Locate every blood parasite and identify its species.
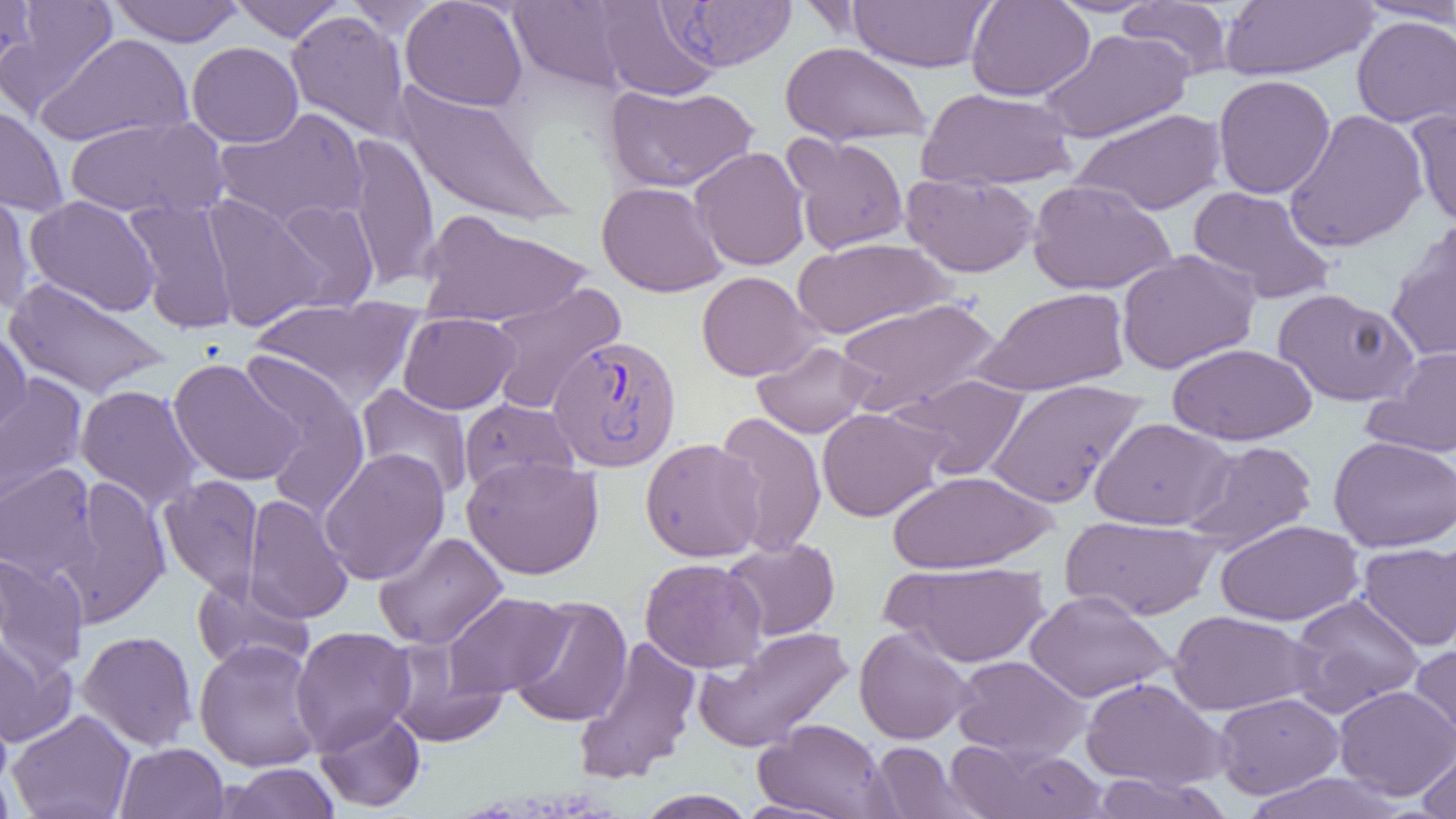

Approximate bounding boxes as (x1, y1, x2, y2) in pixels.
Plasmodium vivax-infected red blood cells: (658, 1, 797, 71), (547, 334, 683, 472).
No Plasmodium falciparum, Plasmodium ovale, Plasmodium malariae, Babesia divergens, or Trypanosoma brucei observed.

Summary:
  - Uninfected red blood cell locations: (0, 0, 39, 81), (2, 0, 118, 117), (109, 0, 243, 46), (229, 0, 346, 41), (400, 0, 528, 111), (508, 0, 635, 94), (966, 0, 1095, 101), (1351, 0, 1456, 25), (344, 1, 447, 38), (594, 1, 722, 101), (852, 1, 1000, 74), (1117, 1, 1236, 80), (1220, 1, 1376, 81), (286, 10, 413, 142), (1352, 15, 1456, 128), (1039, 28, 1193, 143), (36, 33, 193, 147), (187, 41, 303, 148), (780, 42, 931, 146), (1212, 74, 1336, 198), (393, 82, 573, 229), (604, 83, 759, 193), (917, 87, 1078, 190), (0, 102, 68, 216), (213, 107, 370, 231), (1407, 107, 1456, 230), (1071, 108, 1227, 216), (1283, 109, 1428, 252), (64, 116, 226, 219), (344, 132, 439, 291), (783, 133, 910, 255), (690, 146, 810, 271), (781, 154, 1037, 260), (900, 172, 1040, 277), (1027, 179, 1177, 295), (596, 181, 728, 297), (0, 182, 37, 316), (1187, 185, 1337, 305), (202, 194, 328, 331), (25, 196, 162, 316), (123, 199, 240, 333), (269, 199, 379, 312), (418, 210, 592, 328), (1385, 224, 1456, 365), (792, 237, 953, 338), (1116, 249, 1260, 374), (696, 271, 821, 381), (4, 277, 171, 399), (484, 283, 626, 415), (973, 287, 1130, 396), (1273, 288, 1418, 406), (250, 296, 422, 406), (836, 296, 1001, 415), (397, 312, 520, 414), (0, 331, 32, 447), (752, 341, 876, 439), (1166, 342, 1317, 446), (1368, 345, 1456, 458), (238, 350, 371, 512), (168, 358, 305, 487), (893, 373, 1030, 479), (0, 375, 88, 514), (984, 379, 1147, 508), (75, 384, 203, 511), (356, 384, 474, 500), (459, 397, 579, 494), (816, 407, 950, 521), (714, 411, 827, 557), (1090, 417, 1234, 530), (1328, 436, 1456, 552), (640, 438, 766, 562), (1184, 440, 1318, 551), (319, 448, 450, 585), (461, 455, 604, 579), (0, 463, 99, 583), (886, 469, 1056, 573), (159, 475, 265, 600), (58, 477, 171, 625), (242, 494, 354, 624), (1061, 516, 1221, 620), (1216, 519, 1363, 626), (373, 531, 508, 650), (722, 538, 840, 641), (1357, 541, 1455, 650), (0, 552, 89, 677), (640, 557, 767, 673), (883, 561, 1051, 667), (192, 576, 314, 674), (1025, 590, 1175, 702), (442, 592, 573, 698), (1288, 594, 1426, 716), (509, 596, 632, 728), (1168, 610, 1319, 715), (693, 625, 854, 752), (290, 626, 416, 755), (854, 627, 977, 745), (77, 630, 198, 751), (0, 634, 76, 747), (573, 636, 701, 785), (193, 639, 325, 772), (1409, 639, 1456, 753), (385, 640, 508, 747), (951, 655, 1091, 762), (1081, 677, 1229, 791), (1334, 685, 1456, 799), (1213, 692, 1343, 798), (6, 709, 136, 819), (314, 709, 425, 812), (754, 717, 895, 818), (1417, 736, 1456, 819), (115, 742, 229, 819), (869, 742, 976, 818), (946, 742, 1107, 819), (0, 760, 16, 818), (220, 762, 341, 819), (1242, 771, 1405, 818), (1089, 772, 1232, 819), (635, 789, 756, 819)
  - Slide-level diagnosis: Plasmodium vivax
  - Modality: light microscopy
  - Magnification: 1000x
  - Image size: 1456×819 pixels
  - Field of view: one of a larger specimen
  - Preparation: thin blood smear